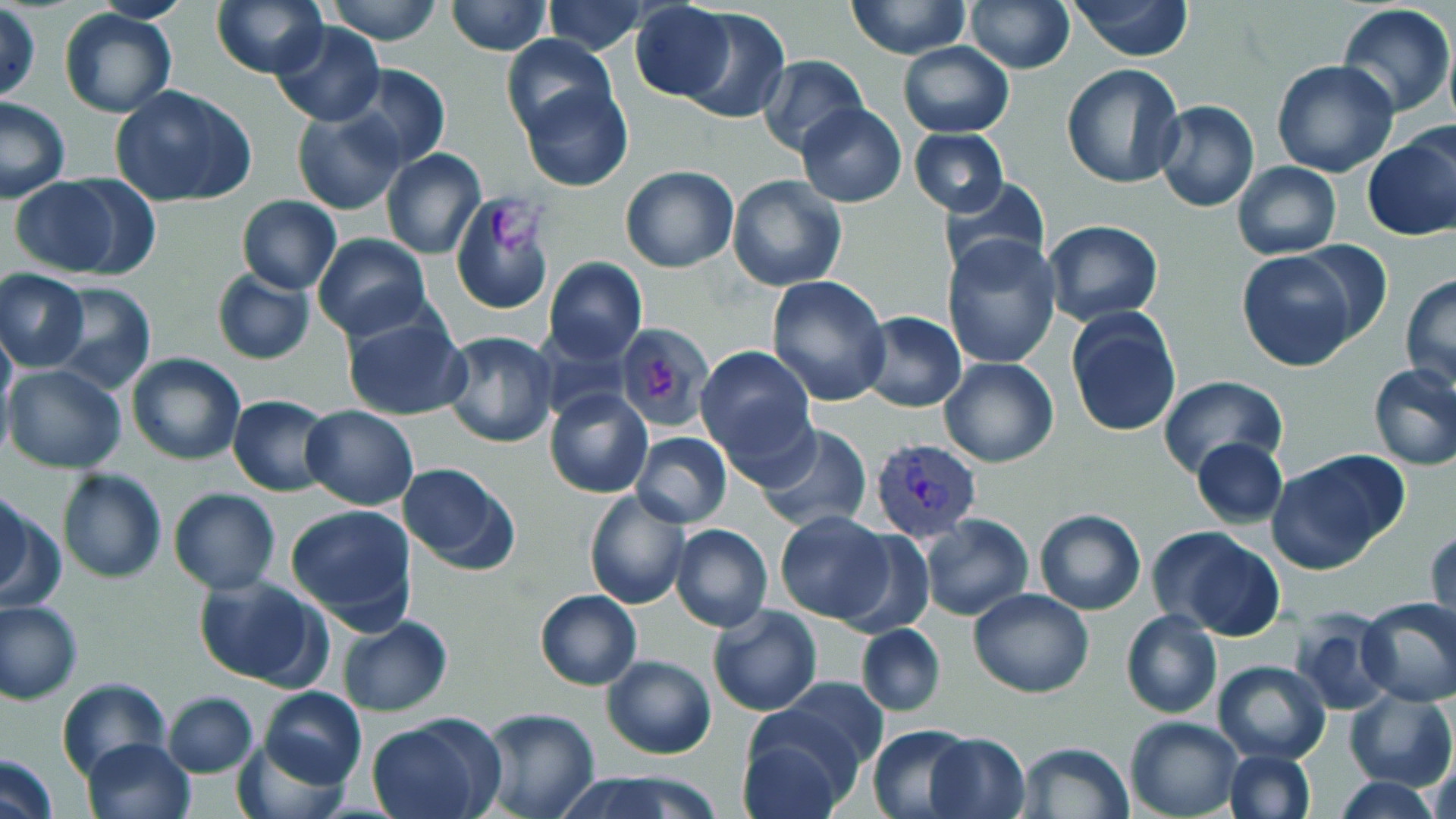
Approximate bounding boxes as (x1,y1)-(x2,y2) corner pairs in pixels. Platelet locations: (491,204)-(548,254), (645,358)-(676,400). Plasmodium vivax-infected red blood cell locations: (870,439)-(981,543). Uninfected red blood cell locations: (210,0)-(326,78), (328,0)-(440,44), (445,0)-(553,56), (846,0)-(972,59), (1065,0)-(1196,60), (541,1)-(650,56), (966,1)-(1075,74), (629,2)-(736,100), (1336,4)-(1455,117), (1,6)-(41,102), (677,7)-(789,125), (59,8)-(177,118), (270,21)-(385,128), (501,34)-(616,143), (898,42)-(1014,138), (756,54)-(868,158), (1271,59)-(1399,178), (343,63)-(452,171), (1062,64)-(1187,190), (519,81)-(634,192), (110,84)-(257,207), (0,96)-(72,204), (1154,101)-(1259,214), (796,103)-(906,205), (292,108)-(405,215), (911,129)-(1008,217), (1363,132)-(1456,242), (381,149)-(487,260), (1231,162)-(1341,259), (620,165)-(738,273), (727,175)-(847,291), (937,175)-(1051,278), (9,177)-(128,276), (450,193)-(557,316), (236,196)-(340,294), (1042,219)-(1162,327), (312,234)-(431,340), (942,234)-(1061,369), (1292,240)-(1394,347), (1236,251)-(1359,370), (544,257)-(646,362), (211,268)-(315,366), (1,270)-(90,372), (1400,274)-(1456,391), (767,275)-(892,407), (47,283)-(156,395), (1065,306)-(1181,439), (341,307)-(473,423), (858,311)-(966,412), (615,322)-(714,431), (0,323)-(15,429), (441,330)-(560,448), (695,345)-(819,470), (126,352)-(247,465), (940,357)-(1058,467), (4,363)-(126,474), (1368,363)-(1456,470), (1158,375)-(1287,477), (545,388)-(653,498), (229,394)-(337,496), (300,405)-(418,510), (753,423)-(871,532), (630,431)-(733,528), (1191,438)-(1288,527), (1270,453)-(1404,573), (397,463)-(520,573), (57,468)-(167,583), (1,488)-(32,599), (583,488)-(692,609), (168,489)-(279,593), (0,493)-(63,611), (285,503)-(416,628), (1034,508)-(1146,614), (773,510)-(895,624), (920,514)-(1033,621), (671,524)-(774,632), (1149,525)-(1286,640), (1427,526)-(1455,634), (834,528)-(934,638), (193,573)-(329,691), (968,589)-(1094,697), (534,590)-(642,691), (1355,595)-(1456,706), (0,601)-(82,704), (708,603)-(822,717), (1290,608)-(1397,715), (1120,610)-(1222,719), (336,616)-(453,716), (856,623)-(946,717), (602,654)-(718,759), (1210,660)-(1330,764), (56,677)-(171,784), (767,678)-(890,782), (258,687)-(366,789), (1345,689)-(1456,791), (161,691)-(258,776), (476,708)-(600,819), (737,713)-(858,817), (364,716)-(498,819), (1126,716)-(1242,819), (866,725)-(978,816), (234,732)-(351,819), (924,732)-(1032,819), (81,737)-(197,819), (1017,742)-(1134,819), (1223,749)-(1316,819), (1426,749)-(1455,819), (0,753)-(60,819), (558,772)-(719,819), (1332,776)-(1445,818). Slide-level diagnosis: Plasmodium vivax. Image is 1456×819 pixels. Thin blood smear. Optical microscopy. 1000x magnification. May-Grünwald-Giemsa stain. One field of a larger specimen.